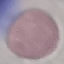

Malaria status: uninfected. Acquired by smartphone through the microscope eyepiece. Giemsa-stained preparation. Cell patch, automatically extracted from a larger field of view and resized to 64 × 64 pixels. Thin blood smear.